Assess this cell for malaria.
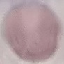
It is uninfected.

Summary:
  - Image type: automatically extracted cell patch, resized to 64 × 64 pixels
  - Preparation: thin smear
  - Stain: Giemsa
  - Capture: smartphone through the microscope eyepiece